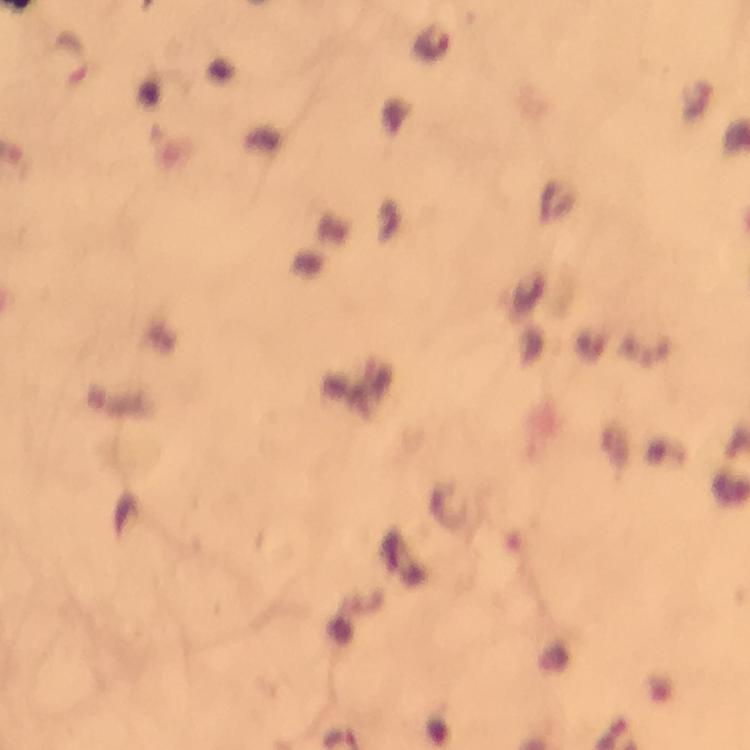

Approximate object centers, in pixels from the top-left corner.
Summary:
  - Plasmodium parasite locations: (x=431, y=43), (x=71, y=56)
  - Magnification: 100x
  - Context: from a malaria diagnostic workup
  - Stain: Giemsa
  - Capture: smartphone camera through the microscope
  - Image size: 750×750 pixels
  - Cropped from: one field of view
  - Immersion oil: applied
  - Preparation: thick smear